Assess this cell for malaria.
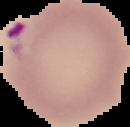
Parasitized.

The area outside the segmented cell region is set to black. From a thin blood smear. Image is 130×127 pixels.